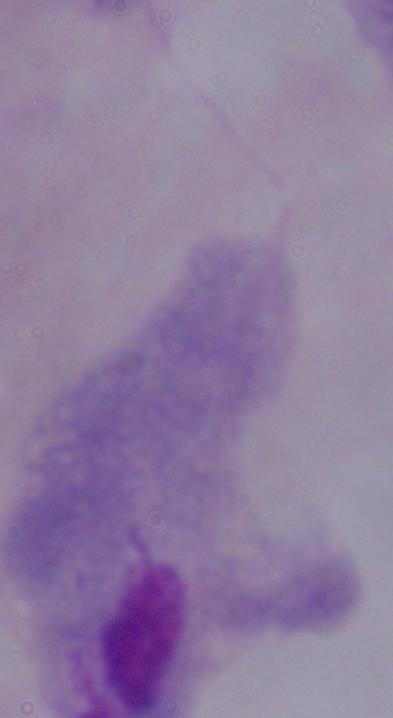
identification = trichomonad
magnification = 1000x
modality = micrograph